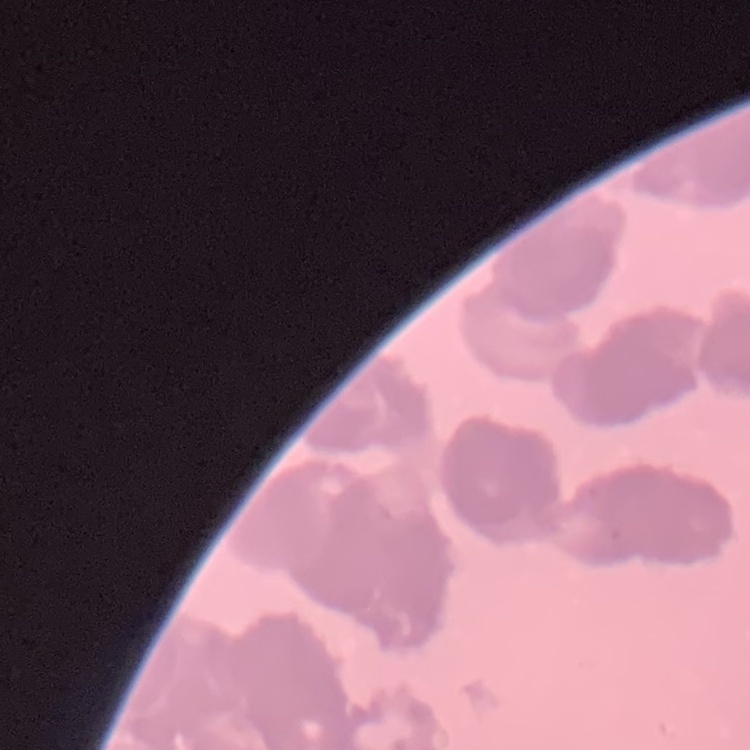
The erythrocytes exhibit rouleaux formation. Square crop of a larger photomicrograph. Thin blood film. Stained with either Field's or Giemsa.